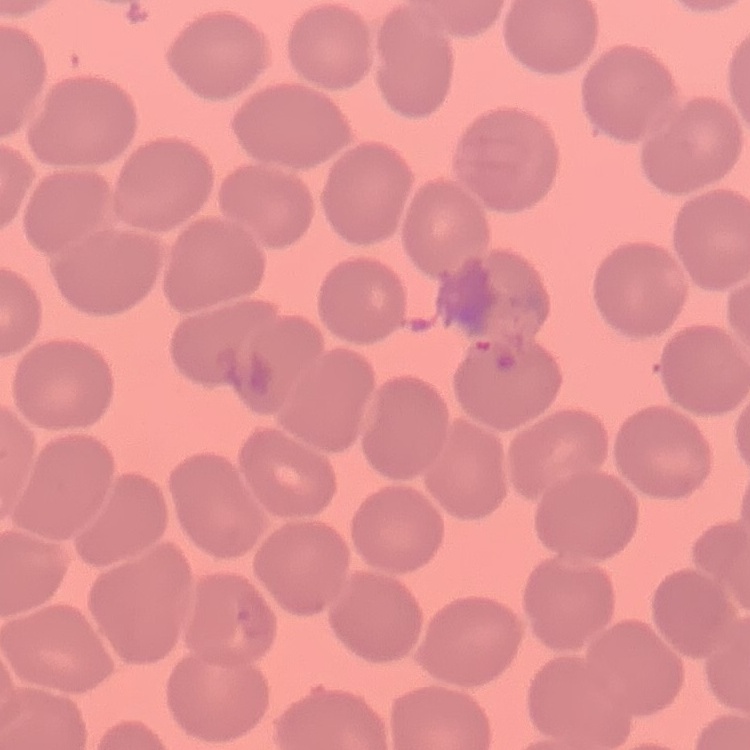
Summary:
  - Red blood cell morphology: no rouleaux formation
  - Preparation: thin blood film
  - Image type: square crop of a larger photomicrograph
  - Stain: Field's or Giemsa